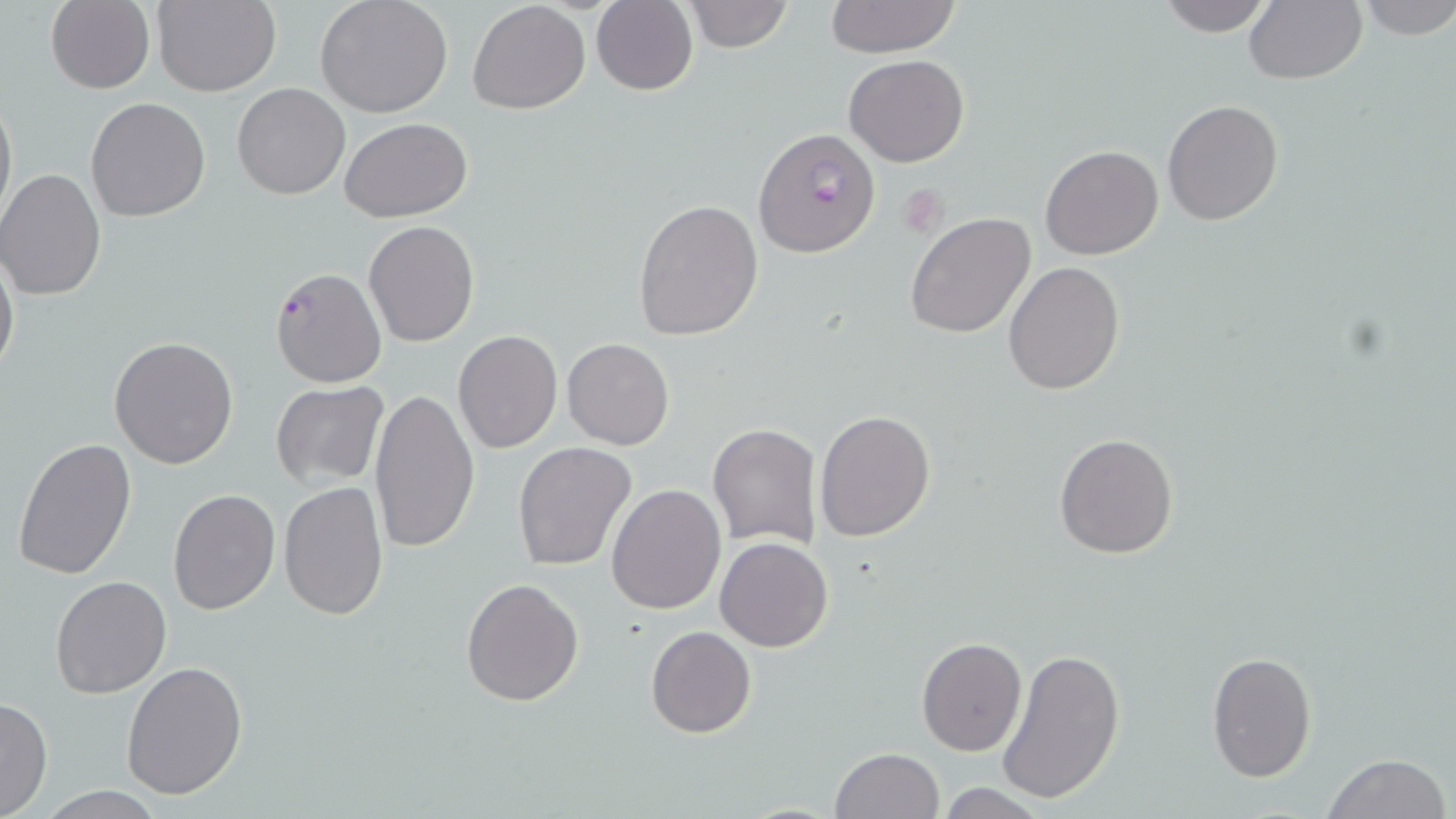

slide-level diagnosis = Plasmodium falciparum
modality = light microscopy
image size = 1456×819 pixels
Plasmodium falciparum-infected red blood cell locations = approximate bounding boxes as (x1,y1)-(x2,y2) corner pairs in pixels: (753,127)-(881,258), (270,265)-(386,389)
field of view = one of a larger specimen
magnification = 1000x
stain = May-Grünwald-Giemsa
preparation = thin blood smear
uninfected red blood cell locations = approximate bounding boxes as (x1,y1)-(x2,y2) corner pairs in pixels: (153,0)-(280,97), (315,0)-(453,119), (684,0)-(795,52), (823,0)-(962,57), (1154,0)-(1275,36), (1243,0)-(1366,83), (1353,0)-(1456,41), (45,1)-(157,94), (467,1)-(591,115), (591,1)-(698,95), (843,56)-(968,168), (232,82)-(349,199), (0,87)-(16,230), (85,97)-(211,223), (1162,99)-(1285,225), (340,118)-(474,220), (1039,143)-(1164,260), (0,169)-(107,301), (633,198)-(765,341), (904,212)-(1037,340), (363,220)-(479,348), (0,247)-(19,384), (1003,261)-(1126,394), (452,330)-(562,454), (109,336)-(240,470), (562,338)-(673,450), (271,381)-(389,490), (370,389)-(478,556), (814,409)-(936,543), (706,422)-(821,551), (1054,433)-(1178,558), (13,437)-(137,581), (512,441)-(635,571), (278,480)-(389,620), (605,484)-(726,613), (168,488)-(281,613), (715,536)-(833,653), (50,574)-(171,698), (461,578)-(584,704), (646,625)-(755,738), (917,636)-(1026,756), (997,647)-(1126,808), (1205,650)-(1316,781), (120,660)-(249,800), (0,698)-(54,818), (829,747)-(944,819), (1320,753)-(1450,819), (930,783)-(1054,817)